Identify the blood parasite species.
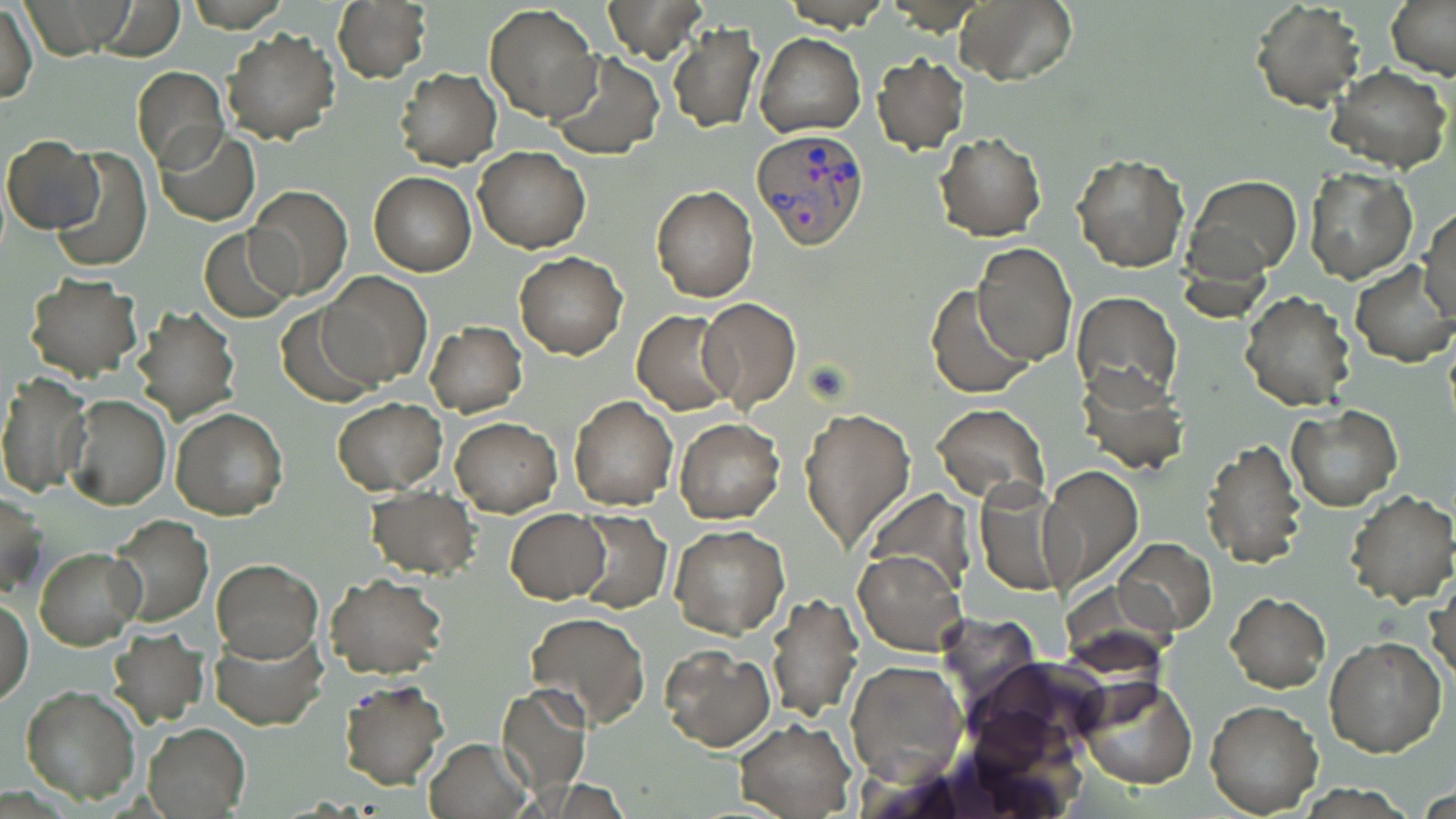

Plasmodium vivax.

Summary:
  - Coordinate format: approximate bounding boxes as [x1, y1, x2, y2] in pixels
  - Uninfected red blood cell locations: [91, 0, 184, 59], [604, 0, 709, 62], [951, 0, 1075, 88], [1386, 0, 1456, 80], [1252, 1, 1364, 110], [1, 2, 38, 105], [332, 2, 431, 82], [483, 4, 601, 124], [667, 23, 764, 133], [222, 29, 340, 144], [756, 34, 866, 138], [549, 51, 664, 160], [871, 56, 968, 153], [1328, 64, 1453, 175], [132, 68, 231, 169], [393, 69, 502, 170], [156, 127, 259, 225], [934, 131, 1046, 241], [3, 136, 105, 235], [50, 147, 152, 271], [474, 147, 591, 252], [1071, 154, 1189, 272], [370, 163, 586, 262], [1301, 165, 1418, 284], [370, 171, 477, 276], [1188, 176, 1302, 277], [245, 185, 352, 299], [652, 185, 757, 302], [1417, 207, 1455, 323], [199, 228, 295, 323], [973, 244, 1077, 366], [515, 252, 627, 359], [1351, 261, 1455, 367], [318, 273, 431, 388], [23, 274, 143, 382], [926, 285, 1034, 399], [1240, 291, 1356, 411], [1069, 292, 1181, 405], [697, 297, 801, 413], [130, 306, 240, 425], [278, 307, 376, 407], [632, 311, 737, 414], [425, 322, 527, 418], [1075, 364, 1188, 476], [0, 371, 90, 497], [65, 395, 171, 510], [569, 395, 678, 511], [332, 398, 447, 493], [933, 402, 1051, 506], [1286, 406, 1401, 511], [170, 407, 288, 519], [801, 407, 916, 554], [451, 417, 560, 514], [674, 419, 784, 522], [1202, 438, 1307, 569], [1037, 464, 1144, 592], [974, 478, 1071, 598], [366, 487, 479, 579], [1345, 490, 1456, 608], [0, 492, 46, 598], [506, 509, 609, 602], [572, 510, 670, 613], [106, 514, 214, 625], [669, 525, 790, 639], [1112, 537, 1217, 636], [36, 546, 145, 650], [854, 551, 965, 656], [211, 559, 321, 661], [323, 573, 449, 680], [1428, 575, 1455, 690], [766, 592, 863, 721], [1225, 593, 1330, 691], [1, 597, 34, 706], [525, 612, 651, 731], [208, 624, 326, 730], [107, 630, 208, 728], [1323, 638, 1448, 757], [660, 646, 775, 750], [845, 658, 966, 786], [1074, 678, 1199, 789], [337, 679, 448, 790], [20, 685, 141, 803], [497, 686, 593, 798], [1206, 700, 1323, 816], [732, 718, 856, 818], [143, 722, 248, 817], [424, 737, 533, 819]
  - Plasmodium vivax-infected red blood cell locations: [751, 128, 868, 248]
  - Modality: light microscopy
  - Preparation: thin blood film
  - Stain: May-Grünwald-Giemsa
  - Magnification: 1000x
  - Image size: 1456×819 pixels
  - Field of view: one of a larger specimen